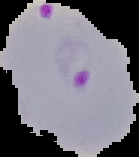
Summary:
  - Preparation: thin blood film
  - Image type: segmented cell region on a black background
  - Result: Plasmodium parasites detected
  - Image size: 139×157 pixels